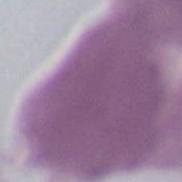
Summary:
  - Identification: erythrocyte
  - Modality: micrograph
  - Magnification: 1000x